Locate every P. falciparum parasite and give its life-cycle stage, and locate every leukocyte and any debris.
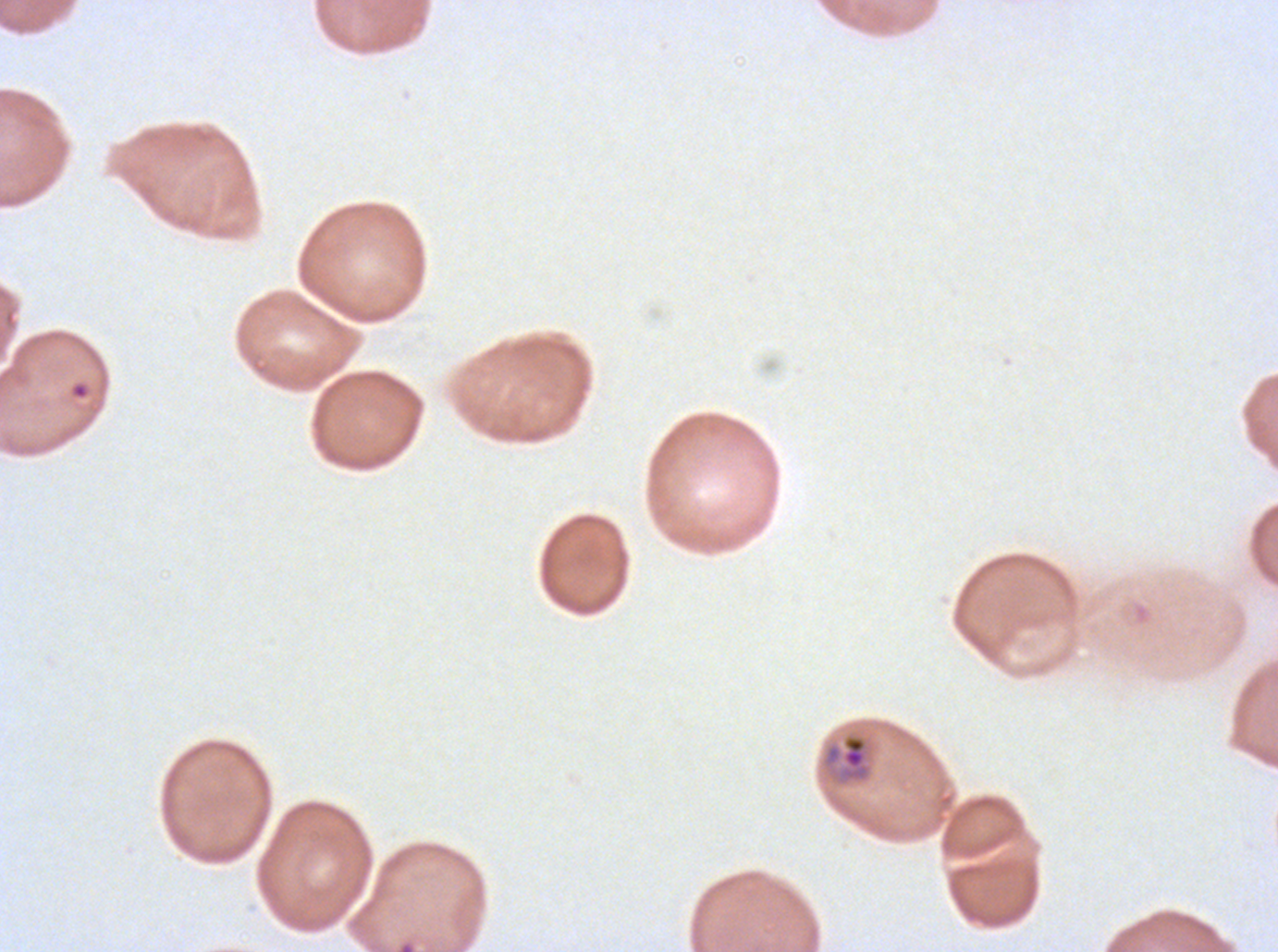

Approximate bounding boxes as {x1, y1, x2, y2} in pixels.
Rings: {69, 382, 90, 400}.
Mid trophozoites: {822, 733, 872, 784}.
No late-ring/early-trophozoite forms, late trophozoites, early schizonts, late schizonts, segmenters, gametocytes, leukocytes, or debris observed.

Summary:
  - Stain: Giemsa
  - Specimen: P. falciparum from a patient in The Gambia, cultured ex vivo for 24 to 48 hours
  - Image size: 1278×952 pixels
  - Life-cycle stages observed: ring, mid trophozoite
  - Preparation: thin blood smear
  - Field of view: sub-image separated from a larger composite